Describe the morphology of the red blood cells.
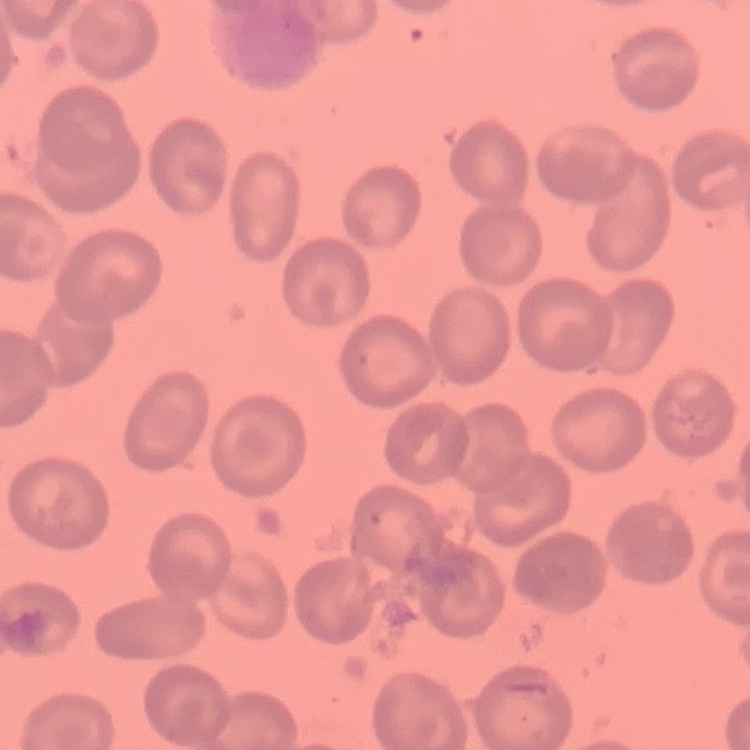

No rouleaux formation.

Summary:
  - Stain: Field's or Giemsa
  - Preparation: thin blood film
  - Image type: one tile cut from a larger photomicrograph